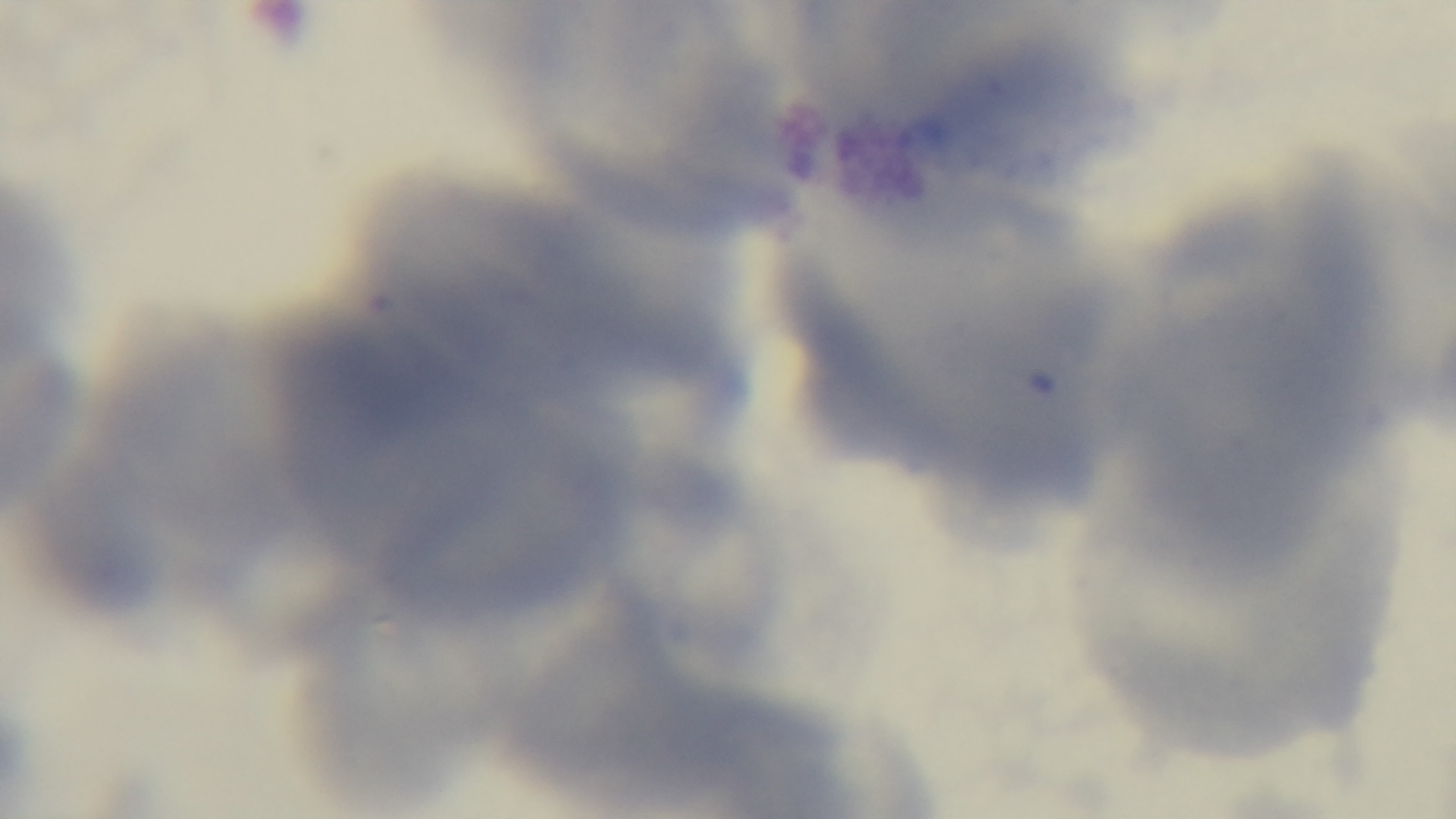

Summary:
  - Field of view: single
  - Stain: Giemsa
  - Preparation: thin blood film
  - Capture: mounted 4K digital camera
  - Modality: light microscopy
  - Objective: 100x oil immersion
  - Malaria status: negative